Identify the parasite.
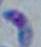

This is Toxoplasma gondii.

magnification: 1000x
modality: photomicrograph